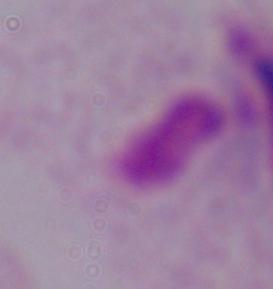
magnification: 1000x
identification: trichomonad
modality: micrograph